Assess this cell for malaria.
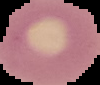
It is uninfected.

Segmented cell region on a black background. From a thin blood smear. Image is 100×85 pixels.